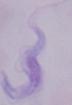
identification = trypanosome
modality = photomicrograph
magnification = 1000x